Report the malaria status of this cell.
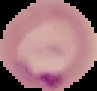

It is parasitized.

Summary:
  - Image type: segmented cell region with the area outside set to black
  - Preparation: thin blood film
  - Image size: 97×91 pixels